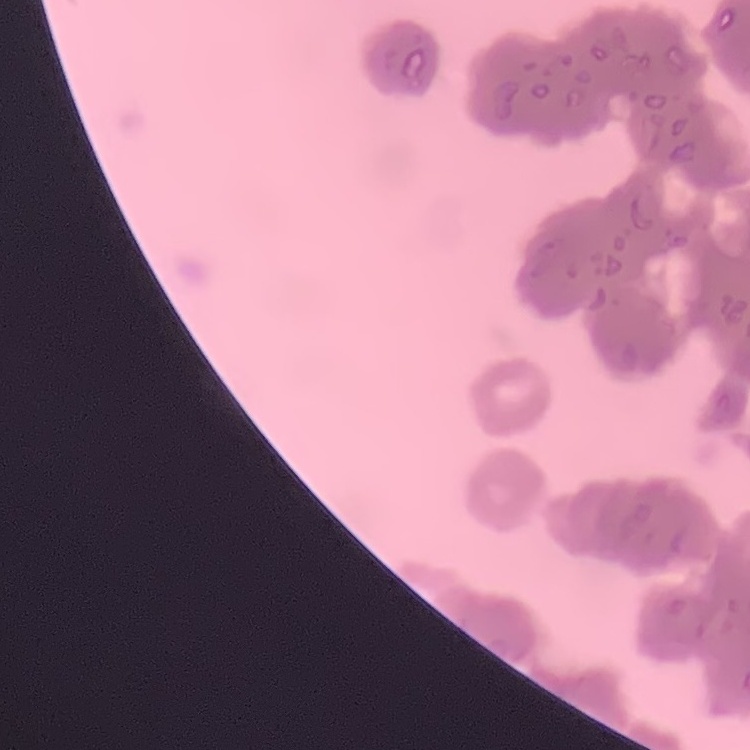
The red blood cells exhibit rouleaux formation. Square crop of a larger photomicrograph. Thin blood film. Field's or Giemsa stain.